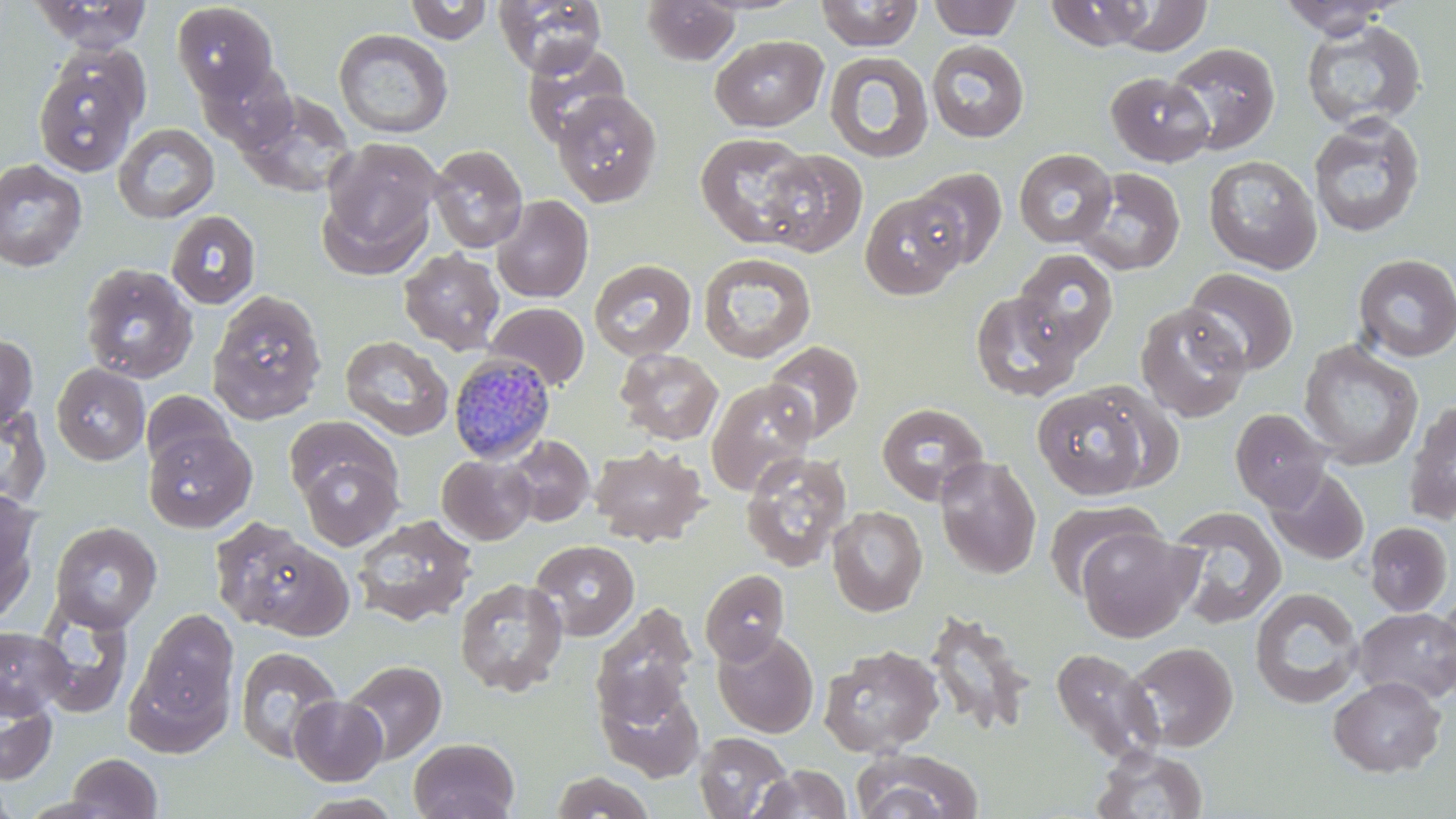
Approximate bounding boxes as (x1,y1)-(x2,y2) corner pairs in pixels. Uninfected red blood cell locations: (493,0)-(607,76), (641,0)-(740,66), (815,0)-(924,51), (928,0)-(1022,41), (1109,0)-(1212,55), (31,1)-(153,54), (404,1)-(492,44), (1044,1)-(1155,51), (1276,1)-(1403,39), (171,2)-(279,100), (1300,19)-(1427,132), (333,28)-(453,139), (710,34)-(828,132), (926,40)-(1030,143), (521,42)-(632,147), (1165,42)-(1279,155), (31,48)-(149,178), (824,51)-(934,164), (200,60)-(300,153), (1106,71)-(1214,166), (238,90)-(357,198), (552,91)-(662,209), (1309,114)-(1426,238), (112,123)-(220,223), (694,132)-(818,249), (318,140)-(442,270), (427,144)-(529,253), (760,149)-(868,257), (1014,149)-(1118,248), (1203,155)-(1323,274), (0,159)-(87,272), (909,167)-(1007,269), (1074,167)-(1186,275), (859,191)-(969,299), (491,195)-(593,303), (165,210)-(261,309), (399,248)-(505,354), (1013,248)-(1119,358), (698,252)-(817,363), (1353,253)-(1456,362), (588,258)-(696,361), (78,262)-(198,384), (1182,268)-(1299,377), (207,290)-(327,424), (970,290)-(1083,402), (485,301)-(590,391), (1135,302)-(1251,422), (0,333)-(38,431), (340,335)-(453,440), (764,340)-(864,443), (1298,340)-(1423,470), (615,348)-(724,445), (51,363)-(150,466), (706,379)-(817,495), (1032,385)-(1155,500), (141,391)-(235,474), (1403,399)-(1456,526), (876,401)-(989,504), (0,403)-(52,511), (1229,408)-(1331,511), (284,415)-(395,503), (144,428)-(256,533), (502,434)-(595,527), (497,435)-(692,533), (589,443)-(709,547), (740,450)-(852,573), (297,453)-(402,550), (437,454)-(537,545), (933,456)-(1042,579), (1265,466)-(1369,565), (0,491)-(40,622), (1044,499)-(1165,598), (827,505)-(928,617), (1166,507)-(1287,630), (350,514)-(478,628), (212,519)-(347,637), (1364,521)-(1453,616), (49,522)-(162,633), (1077,525)-(1200,643), (530,539)-(639,640), (700,567)-(791,666), (454,578)-(568,696), (1249,587)-(1365,709), (1435,588)-(1456,693), (33,602)-(133,719), (592,602)-(699,725), (1354,606)-(1456,704), (131,607)-(240,743), (924,609)-(1035,738), (0,625)-(72,719), (712,629)-(818,738), (1124,641)-(1238,752), (819,644)-(944,758), (235,646)-(342,762), (1050,646)-(1163,763), (341,659)-(447,764), (1328,675)-(1447,777), (596,677)-(705,783), (0,685)-(59,786), (289,696)-(388,785), (693,731)-(792,818), (409,738)-(520,819), (1090,745)-(1209,819), (850,748)-(985,819), (66,752)-(163,818), (751,765)-(852,818), (550,770)-(656,818), (0,779)-(20,819), (291,793)-(407,819). Plasmodium malariae-infected red blood cell locations: (448,353)-(556,464). Slide-level diagnosis: Plasmodium malariae. Thin blood film. May-Grünwald-Giemsa-stained preparation. Image is 1456×819 pixels. Light microscopy. Captured at 1000x magnification. Single field of view.